Describe the morphology of the erythrocytes.
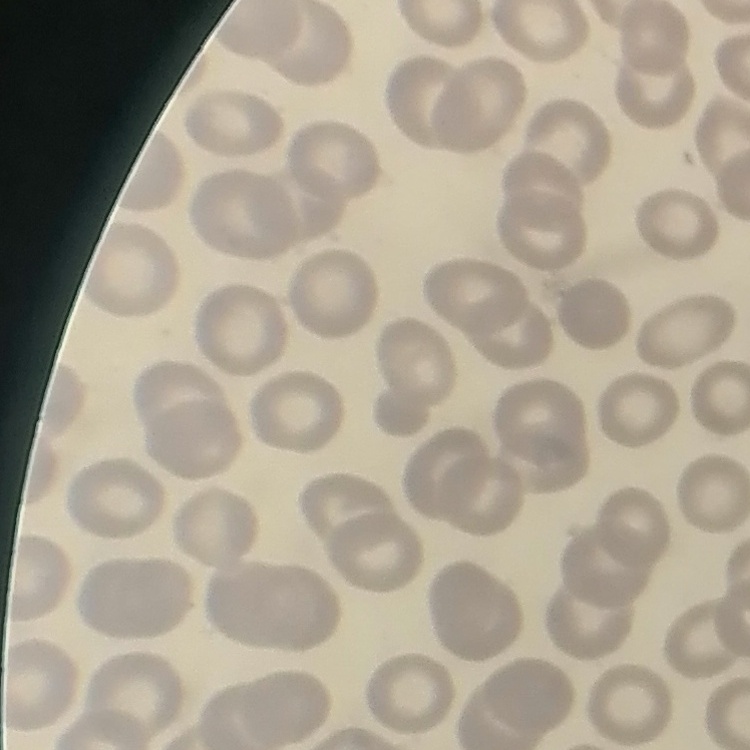

They show no rouleaux formation.

One tile cut from a larger photomicrograph. Thin peripheral smear. Stained with either Field's or Giemsa.